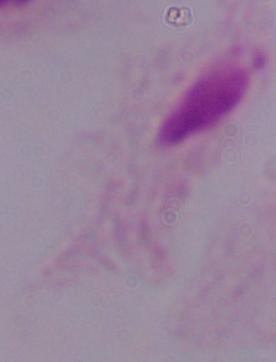

A trichomonad is shown. Photomicrograph. Captured at 1000x magnification.